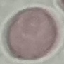

malaria_status: uninfected
stain: Giemsa
image_type: cell patch, automatically extracted from a larger field of view and resized to 64 × 64 pixels
capture: smartphone camera at the microscope eyepiece
preparation: thin blood smear